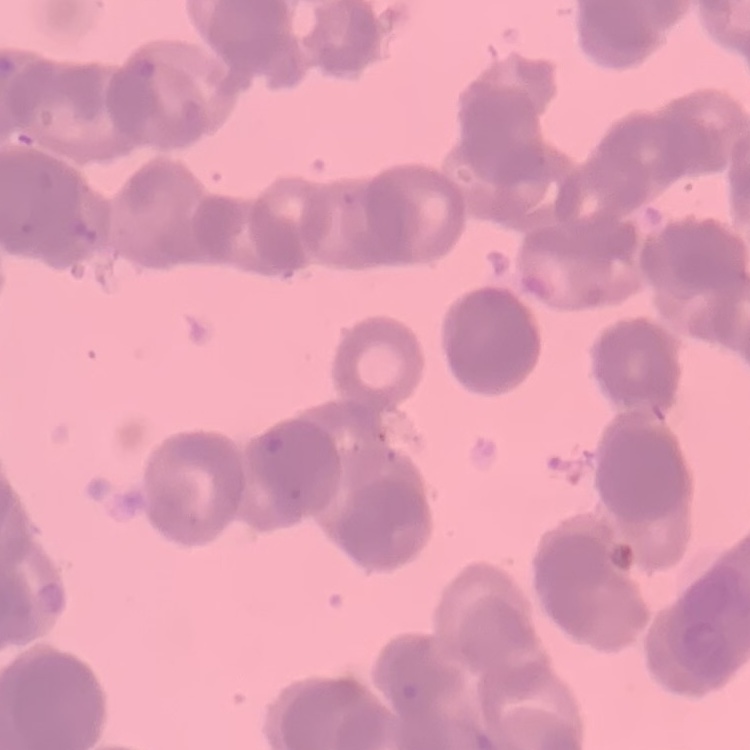

The red blood cells show rouleaux formation. Stained with either Field's or Giemsa. One tile cut from a larger photomicrograph. Thin blood smear.